Describe the morphology of the erythrocytes.
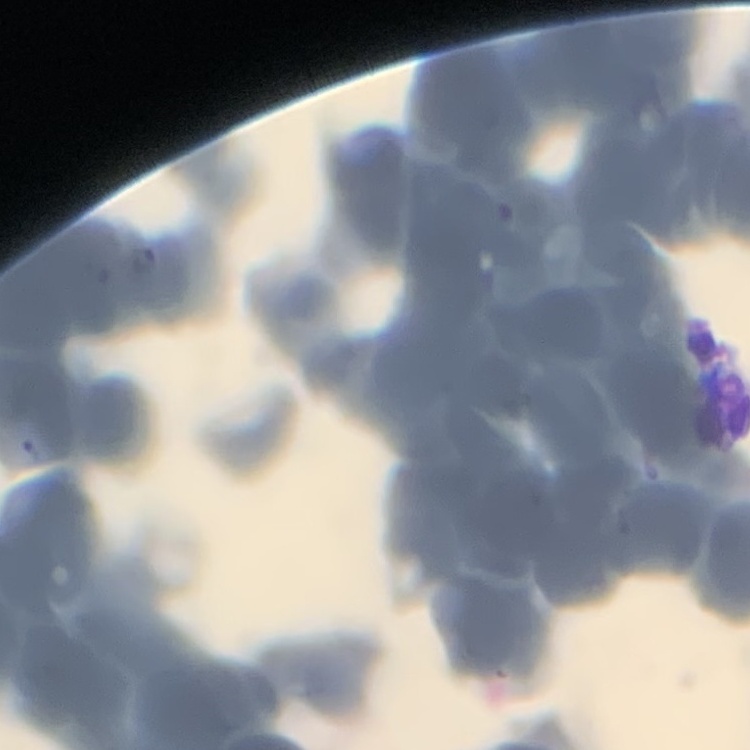
They show rouleaux formation.

Thin blood smear. Field's or Giemsa stain. One tile cut from a larger photomicrograph.